Identify the cell.
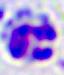
This is a leukocyte.

Captured at 400x magnification. Photomicrograph.